Point out each leukocyte.
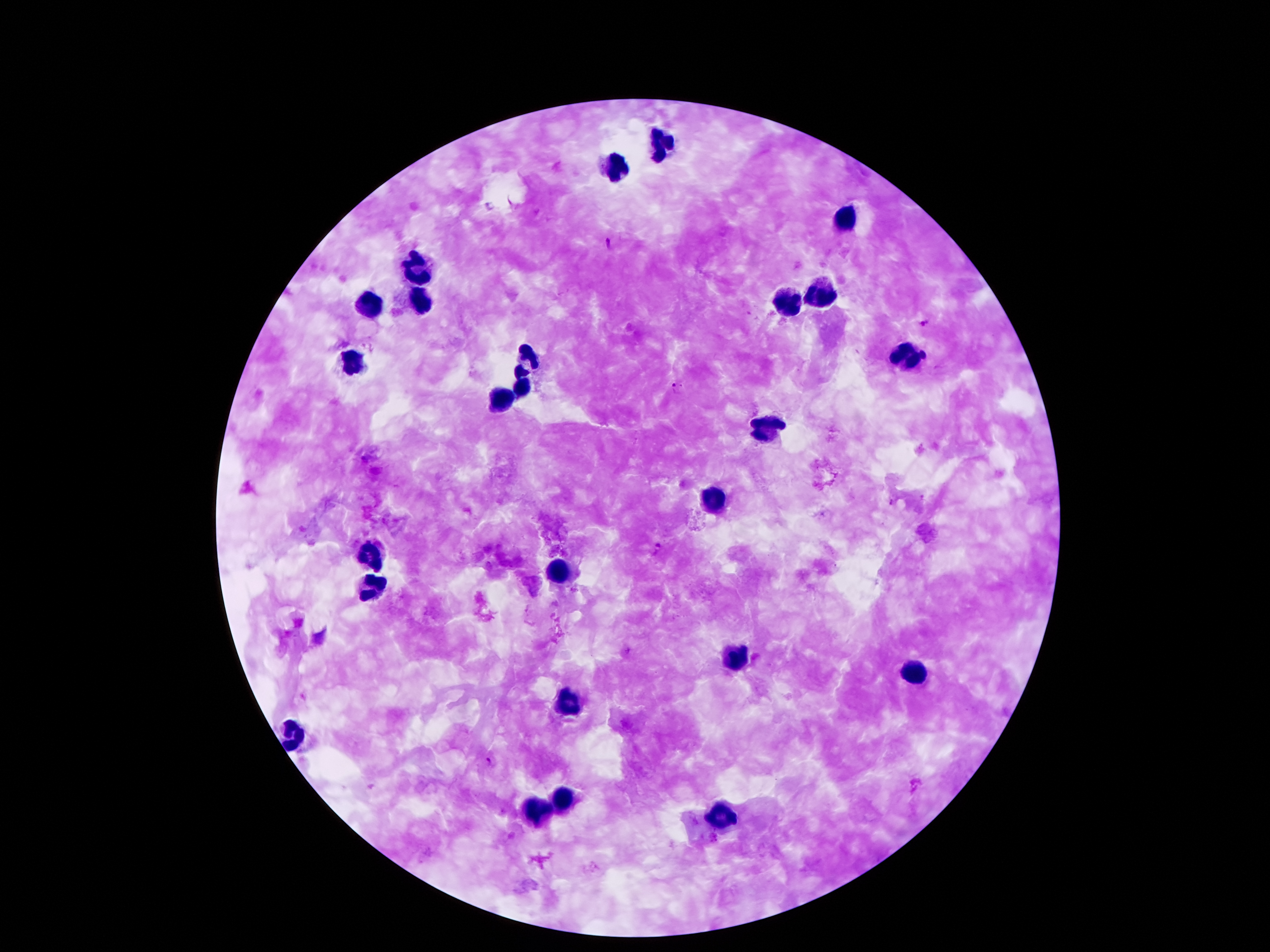

Approximate centers as [x, y] in pixels.
Leukocytes: [660, 142], [613, 163], [842, 216], [414, 272], [821, 296], [414, 303], [788, 303], [370, 309], [903, 358], [529, 359], [354, 363], [524, 389], [500, 403], [771, 429], [713, 502], [375, 555], [557, 569], [370, 593], [737, 655], [913, 675], [567, 706], [294, 737], [560, 802], [538, 809], [720, 816].

Summary:
  - Malaria parasite locations: [490, 207], [611, 242], [924, 322], [924, 353], [673, 385], [658, 547], [489, 761]
  - Capture: smartphone camera through the microscope eyepiece
  - Patient malaria status: infected with Plasmodium falciparum
  - Magnification: 100x
  - Image size: 1270×952 pixels
  - Preparation: thick blood smear
  - Stain: Giemsa
  - Field of view: single